Identify the blood parasite species.
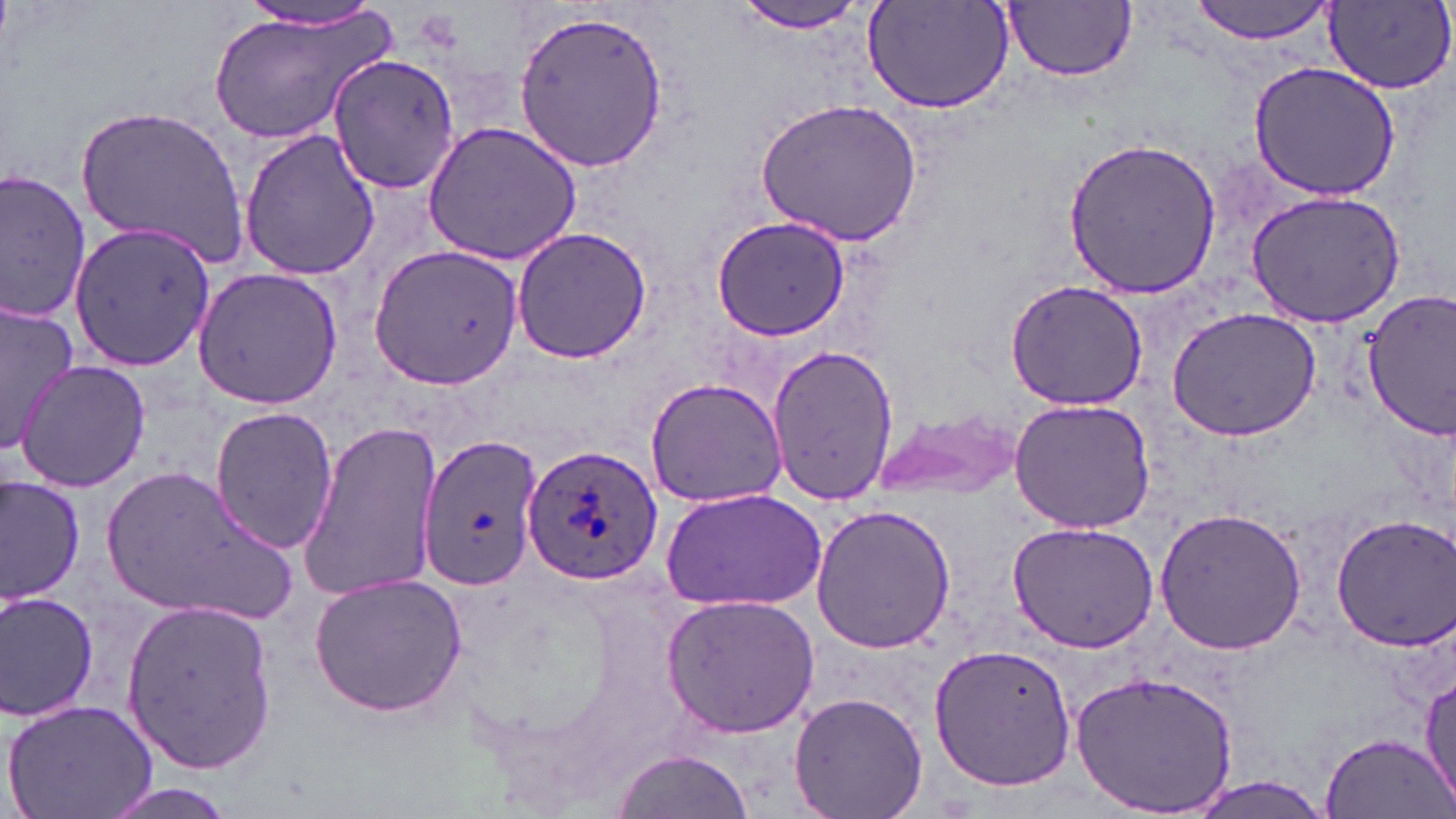
Plasmodium ovale.

{
  "magnification": "1000x",
  "uninfected_red_blood_cell_locations": "approximate bounding boxes as named x1/y1/x2/y2 corners in pixels: (x1=727, y1=0, x2=883, y2=34), (x1=864, y1=0, x2=1017, y2=116), (x1=1190, y1=0, x2=1336, y2=44), (x1=210, y1=1, x2=391, y2=147), (x1=1005, y1=2, x2=1138, y2=82), (x1=236, y1=3, x2=388, y2=33), (x1=1326, y1=3, x2=1456, y2=97), (x1=511, y1=9, x2=669, y2=171), (x1=329, y1=55, x2=461, y2=194), (x1=1249, y1=61, x2=1398, y2=198), (x1=757, y1=97, x2=922, y2=246), (x1=76, y1=104, x2=248, y2=263), (x1=423, y1=121, x2=583, y2=265), (x1=239, y1=127, x2=380, y2=282), (x1=1063, y1=137, x2=1222, y2=299), (x1=0, y1=169, x2=93, y2=326), (x1=1246, y1=190, x2=1407, y2=325), (x1=710, y1=216, x2=850, y2=342), (x1=67, y1=221, x2=220, y2=367), (x1=510, y1=227, x2=652, y2=365), (x1=367, y1=241, x2=526, y2=388), (x1=190, y1=265, x2=343, y2=410), (x1=1005, y1=281, x2=1149, y2=410), (x1=1362, y1=289, x2=1456, y2=439), (x1=0, y1=295, x2=77, y2=446), (x1=1166, y1=306, x2=1322, y2=440), (x1=766, y1=343, x2=897, y2=505), (x1=14, y1=359, x2=150, y2=493), (x1=645, y1=377, x2=787, y2=508), (x1=1007, y1=399, x2=1156, y2=534), (x1=208, y1=406, x2=339, y2=554), (x1=874, y1=410, x2=1022, y2=499), (x1=296, y1=419, x2=445, y2=599), (x1=415, y1=432, x2=546, y2=593), (x1=98, y1=467, x2=293, y2=623), (x1=1, y1=474, x2=85, y2=608), (x1=659, y1=486, x2=827, y2=610), (x1=809, y1=504, x2=956, y2=655), (x1=1153, y1=509, x2=1310, y2=656), (x1=1328, y1=514, x2=1456, y2=651), (x1=1006, y1=520, x2=1161, y2=652), (x1=309, y1=574, x2=467, y2=719), (x1=1, y1=591, x2=101, y2=724), (x1=660, y1=592, x2=820, y2=737), (x1=122, y1=599, x2=278, y2=775), (x1=928, y1=642, x2=1077, y2=792), (x1=1418, y1=667, x2=1454, y2=813), (x1=1072, y1=669, x2=1239, y2=819), (x1=789, y1=692, x2=927, y2=819), (x1=3, y1=698, x2=159, y2=819), (x1=1323, y1=732, x2=1451, y2=818), (x1=608, y1=749, x2=754, y2=819)",
  "plasmodium_ovale_infected_red_blood_cell_locations": "approximate bounding boxes as named x1/y1/x2/y2 corners in pixels: (x1=521, y1=439, x2=666, y2=583)",
  "image_size": "1456×819 pixels",
  "field_of_view": "one of a larger specimen",
  "modality": "optical microscopy",
  "stain": "May-Grünwald-Giemsa",
  "preparation": "thin blood film"
}